Point out each Plasmodium parasite.
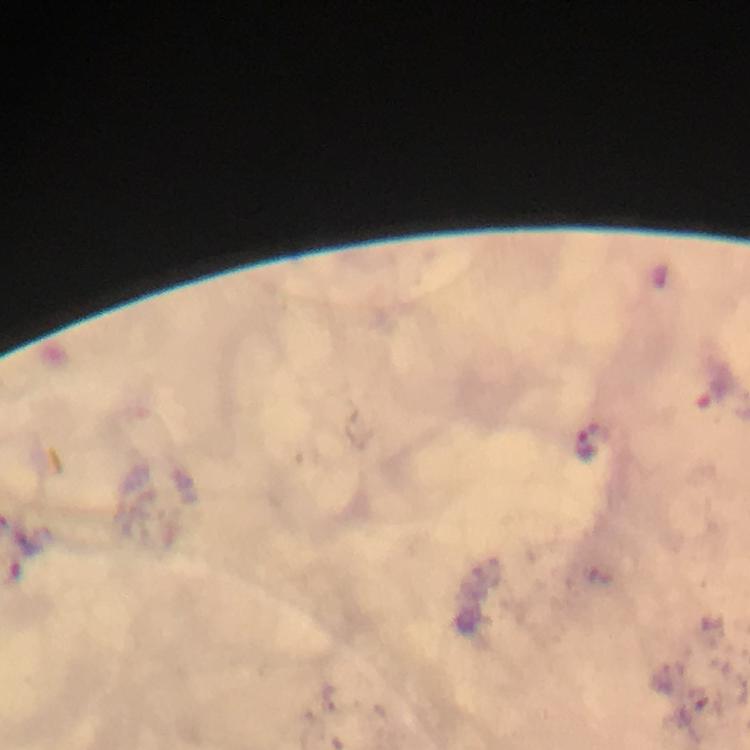

Approximate centers as (x, y) in pixels.
Plasmodium parasites: (584, 444).

preparation = thick smear
stain = Giemsa
immersion oil = applied
image size = 750×750 pixels
capture = smartphone photograph through a microscope
magnification = 100x
cropped from = one field of view
context = from a diagnostic examination for malaria